State which parasite is depicted.
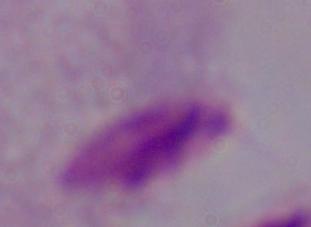
This is a trichomonad.

Captured at 1000x magnification. Micrograph.